Classify the preparation.
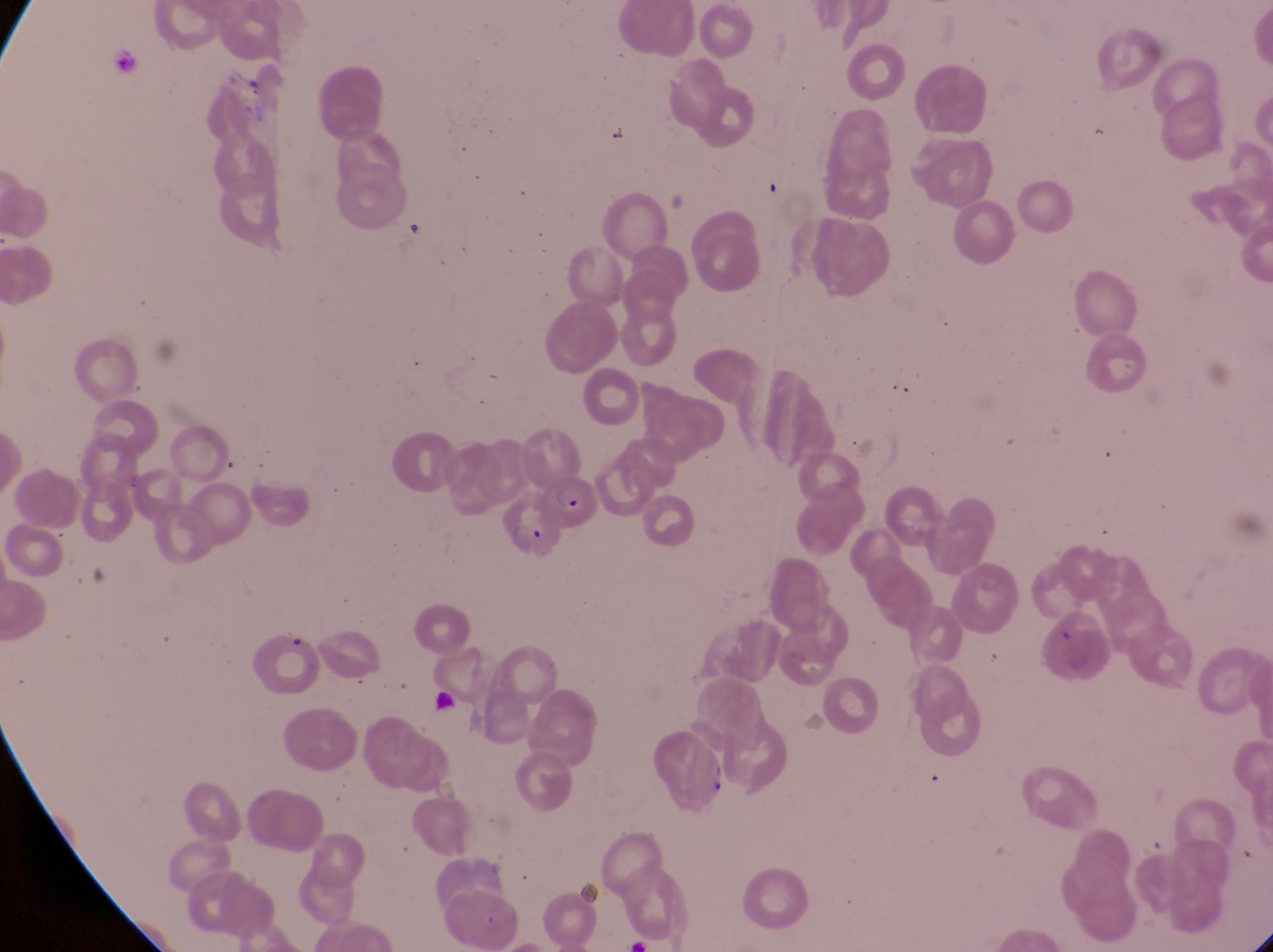
Thin blood film.

country = Uganda
capture = smartphone photograph through the eyepiece of an Olympus CX-23 microscope
field of view = single
image size = 1273×952 pixels
artifact (platelet-like body, stain precipitate, or debris) locations = approximate bounding boxes as left top right bottom in pixels: 426 681 473 741; 697 754 736 796
parasitised red blood cell locations = approximate bounding boxes as left top right bottom in pixels: 539 475 596 528
magnification = 1000x